Report the malaria status of this cell.
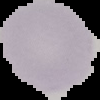

Uninfected.

image_size: 100×100 pixels
preparation: thin blood smear
image_type: segmented cell region on a black background